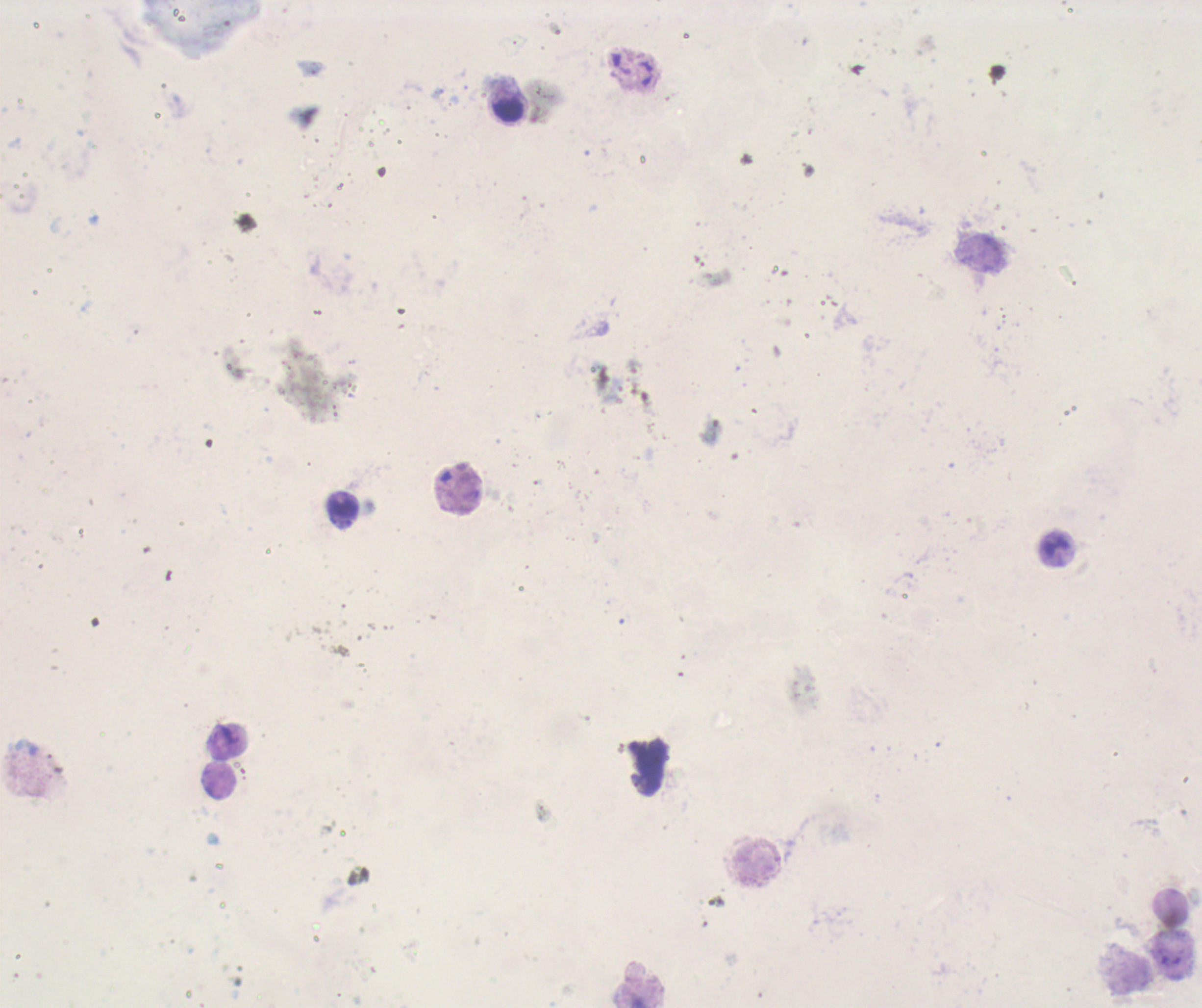
coordinate format = approximate centers as (x, y) in pixels
leukocyte locations = (506, 108), (338, 506)
context = previously used in an actual diagnosis
stain = Romanowsky
image size = 1202×1008 pixels
coloration quality = bad
preparation = thick blood smear
magnification = 100x
background quality = unsatisfactory
result = no Plasmodium parasites detected
field of view = single